Assess this cell for malaria.
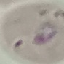
It is parasitized.

Cell patch, automatically extracted from a larger field of view and resized to 64 × 64 pixels. Giemsa stain. Thin smear of blood. Acquired by smartphone through the microscope eyepiece.